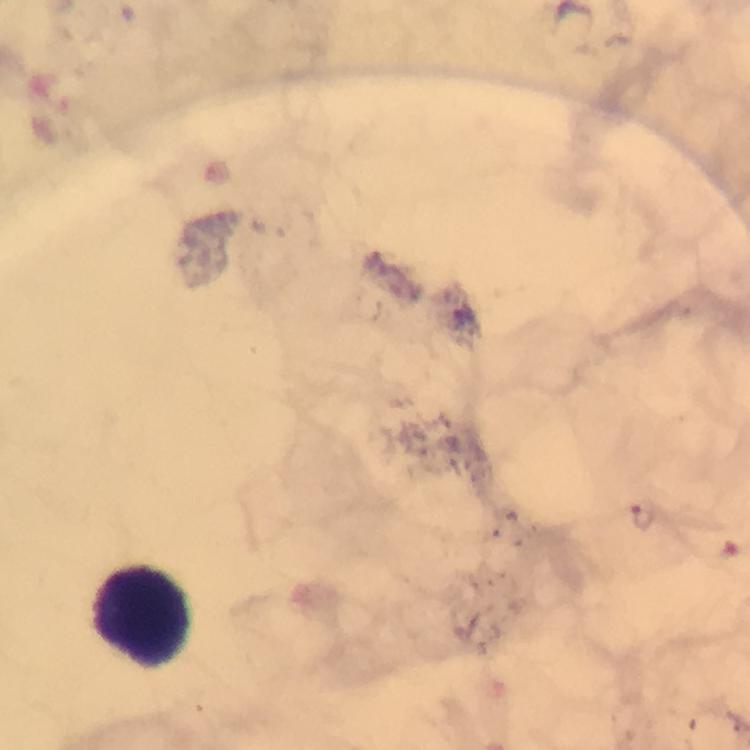
leukocyte locations = approximate centers as {x, y} in pixels: {149, 616}
context = from a diagnostic examination for malaria
magnification = 100x
malaria parasite locations = approximate centers as {x, y} in pixels: {642, 518}
cropped from = one field of view
stain = Giemsa
capture = smartphone camera through the microscope
preparation = thick smear
immersion oil = used
image size = 750×750 pixels